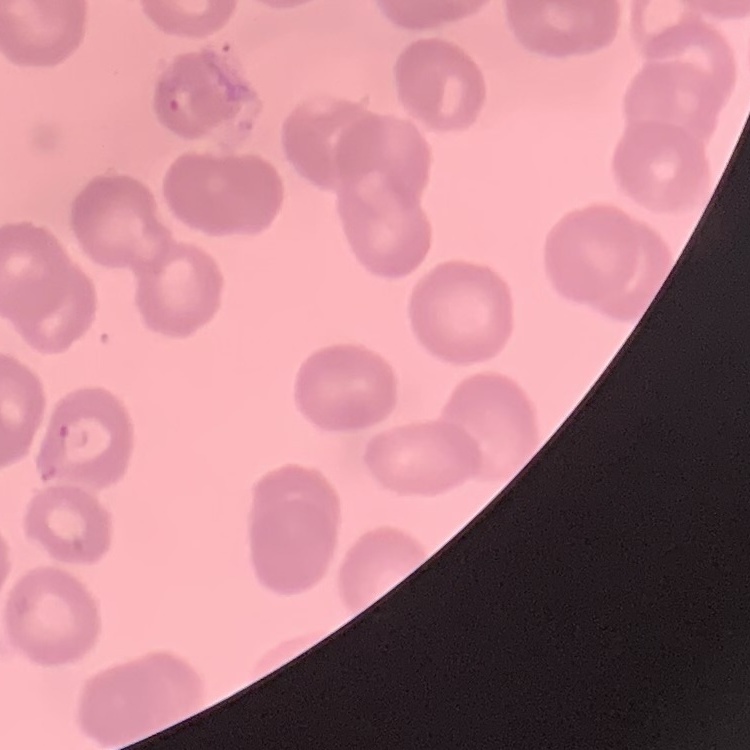
The erythrocytes show no rouleaux formation. One tile cut from a larger photomicrograph. Thin peripheral smear. Field's or Giemsa stain.